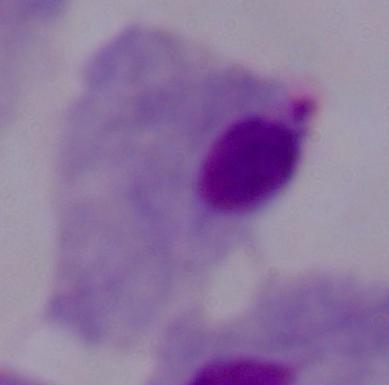
modality = micrograph
magnification = 1000x
identification = trichomonad